Identify the cell.
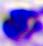

A leukocyte.

Summary:
  - Magnification: 400x
  - Modality: photomicrograph